Assess the morphology of the erythrocytes.
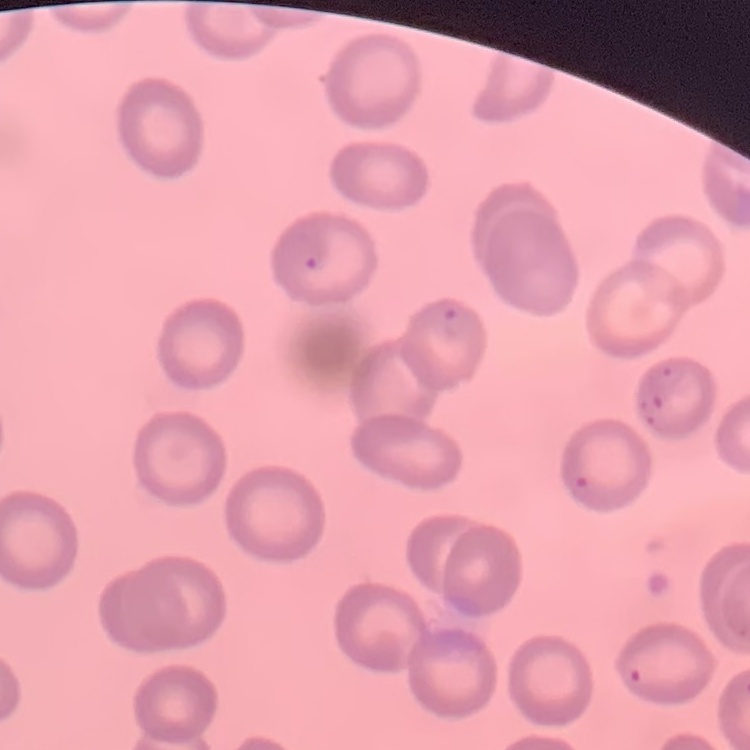

They show no rouleaux formation.

image type = one tile cut from a larger photomicrograph
stain = Field's or Giemsa
preparation = thin blood smear